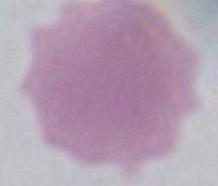

An erythrocyte is shown. 1000x magnification. Photomicrograph.